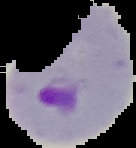
Result: Plasmodium parasites identified. The area outside the segmented cell region is set to black. From a thin blood film. Image is 136×148 pixels.